Report the malaria status.
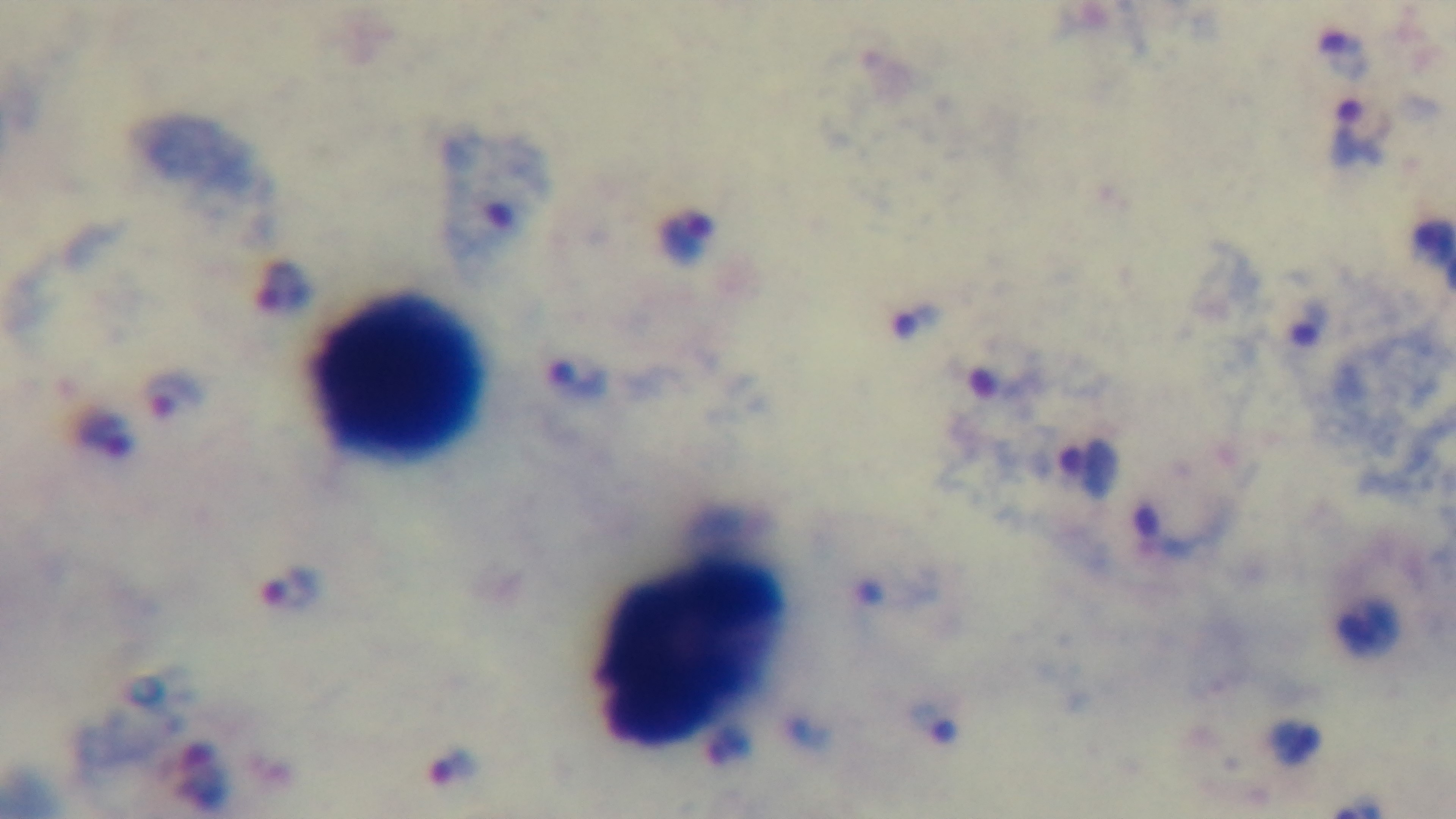
It is infected.

Preparation: thick blood film. Light microscopy. Giemsa stain. Single field of view. 100x oil-immersion objective. Mounted 4K digital camera.